Assess this cell for malaria.
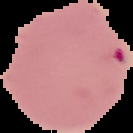
Parasitized.

Image is 133×133 pixels. Segmented cell region on a black background. From a thin blood smear.